Describe the morphology of the red blood cells.
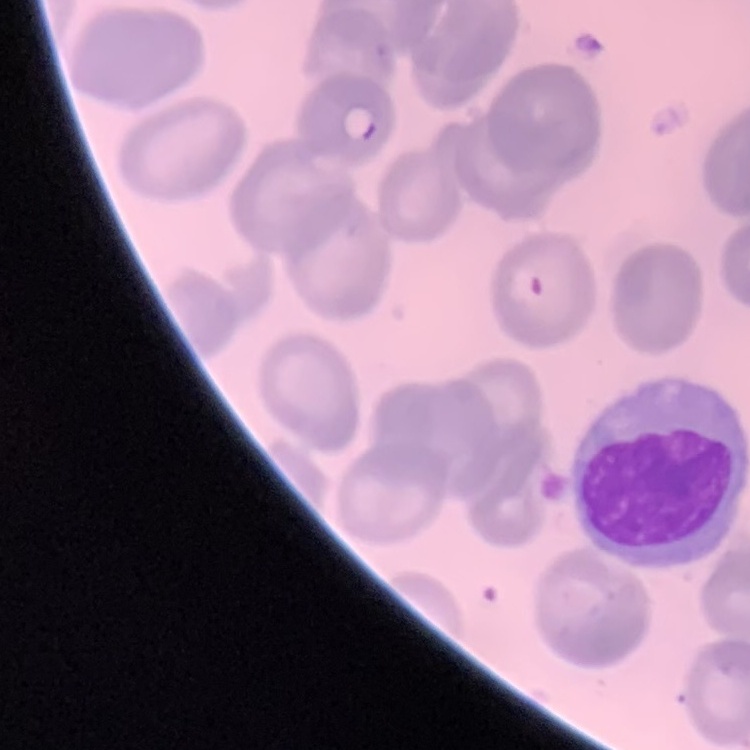

No rouleaux formation.

Thin blood film. Stained with either Field's or Giemsa. One tile cut from a larger photomicrograph.